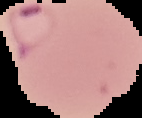
Summary:
  - Preparation: thin blood smear
  - Image type: segmented cell region with the area outside set to black
  - Image size: 142×118 pixels
  - Malaria status: parasitized